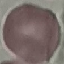
{
  "result": "no malaria parasites detected",
  "capture": "smartphone through the microscope eyepiece",
  "stain": "Giemsa",
  "preparation": "thin blood smear",
  "image_type": "automatically extracted cell patch, resized to 64 × 64 pixels"
}